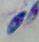
identification: Toxoplasma gondii
modality: micrograph
magnification: 1000x